Outline each uninfected red blood cell.
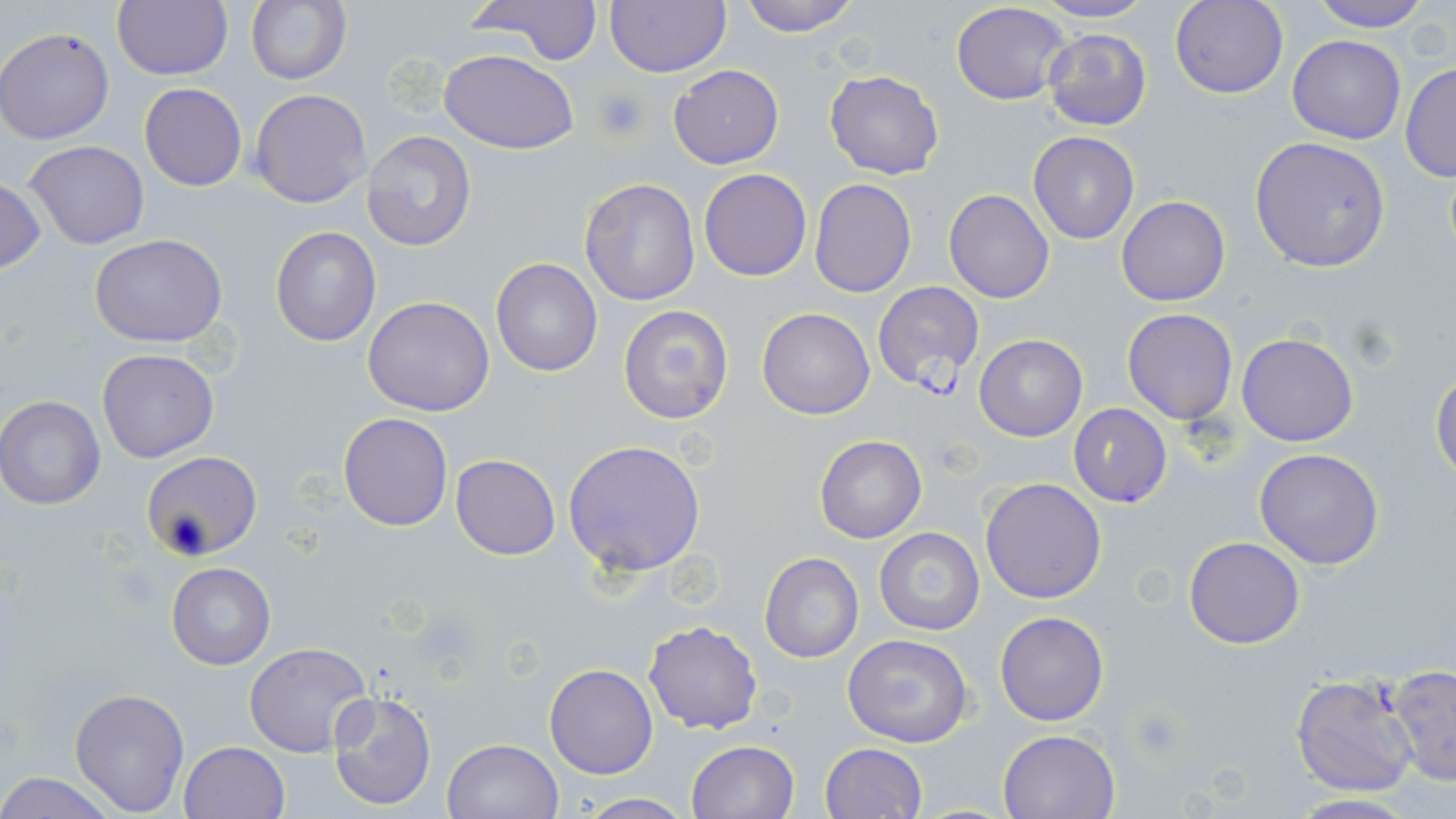
Approximate bounding boxes as [x1, y1, x2, y2] in pixels.
Uninfected red blood cells: [114, 0, 232, 80], [246, 0, 352, 87], [468, 0, 599, 66], [605, 0, 729, 77], [738, 0, 862, 35], [1306, 0, 1436, 31], [1034, 1, 1154, 25], [1170, 1, 1289, 99], [951, 2, 1071, 106], [1, 27, 114, 144], [1042, 29, 1152, 131], [1286, 34, 1406, 144], [439, 49, 578, 155], [1400, 63, 1456, 183], [667, 64, 783, 168], [824, 70, 944, 179], [139, 82, 247, 191], [250, 89, 372, 209], [362, 130, 476, 250], [1027, 131, 1140, 245], [1248, 136, 1392, 272], [24, 140, 149, 249], [699, 168, 812, 281], [0, 176, 46, 278], [578, 177, 703, 306], [809, 178, 916, 297], [944, 189, 1055, 304], [1116, 196, 1230, 306], [271, 226, 381, 346], [90, 236, 227, 348], [491, 257, 603, 377], [363, 296, 495, 417], [619, 303, 736, 425], [758, 308, 874, 420], [1122, 309, 1237, 425], [1236, 332, 1359, 447], [974, 334, 1087, 441], [97, 348, 218, 461], [1430, 368, 1456, 484], [0, 394, 109, 509], [338, 412, 454, 531], [814, 433, 927, 543], [563, 439, 707, 577], [1253, 448, 1385, 569], [142, 451, 262, 558], [451, 454, 560, 560], [979, 478, 1107, 604], [874, 527, 986, 636], [1183, 535, 1305, 649], [759, 552, 863, 662], [167, 562, 274, 670], [994, 610, 1110, 726], [642, 619, 763, 735], [842, 633, 974, 748], [244, 642, 373, 756], [545, 663, 658, 779], [1388, 666, 1455, 785], [1288, 672, 1419, 797], [69, 686, 191, 816], [326, 689, 438, 811], [998, 728, 1120, 819], [441, 738, 564, 819], [177, 740, 289, 819], [685, 740, 798, 819], [820, 742, 928, 819], [0, 773, 118, 817], [572, 793, 694, 817], [1283, 793, 1422, 818].

Summary:
  - Platelet locations: [594, 87, 648, 141], [1130, 706, 1185, 760]
  - Plasmodium falciparum-infected red blood cell locations: [874, 286, 986, 396], [1067, 403, 1173, 508]
  - Slide-level diagnosis: Plasmodium falciparum
  - Modality: optical microscopy
  - Magnification: 1000x
  - Field of view: one of a larger specimen
  - Stain: May-Grünwald-Giemsa
  - Preparation: thin blood smear
  - Image size: 1456×819 pixels